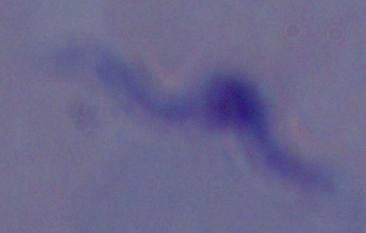

Photomicrograph. A trypanosome is shown. Captured at 1000x magnification.